Report the malaria status of this cell.
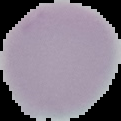
Uninfected.

Segmented cell region on a black background. Image is 121×121 pixels. From a thin blood smear.